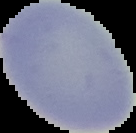
malaria status = uninfected
preparation = thin blood film
image size = 136×133 pixels
image type = segmented cell region on a black background